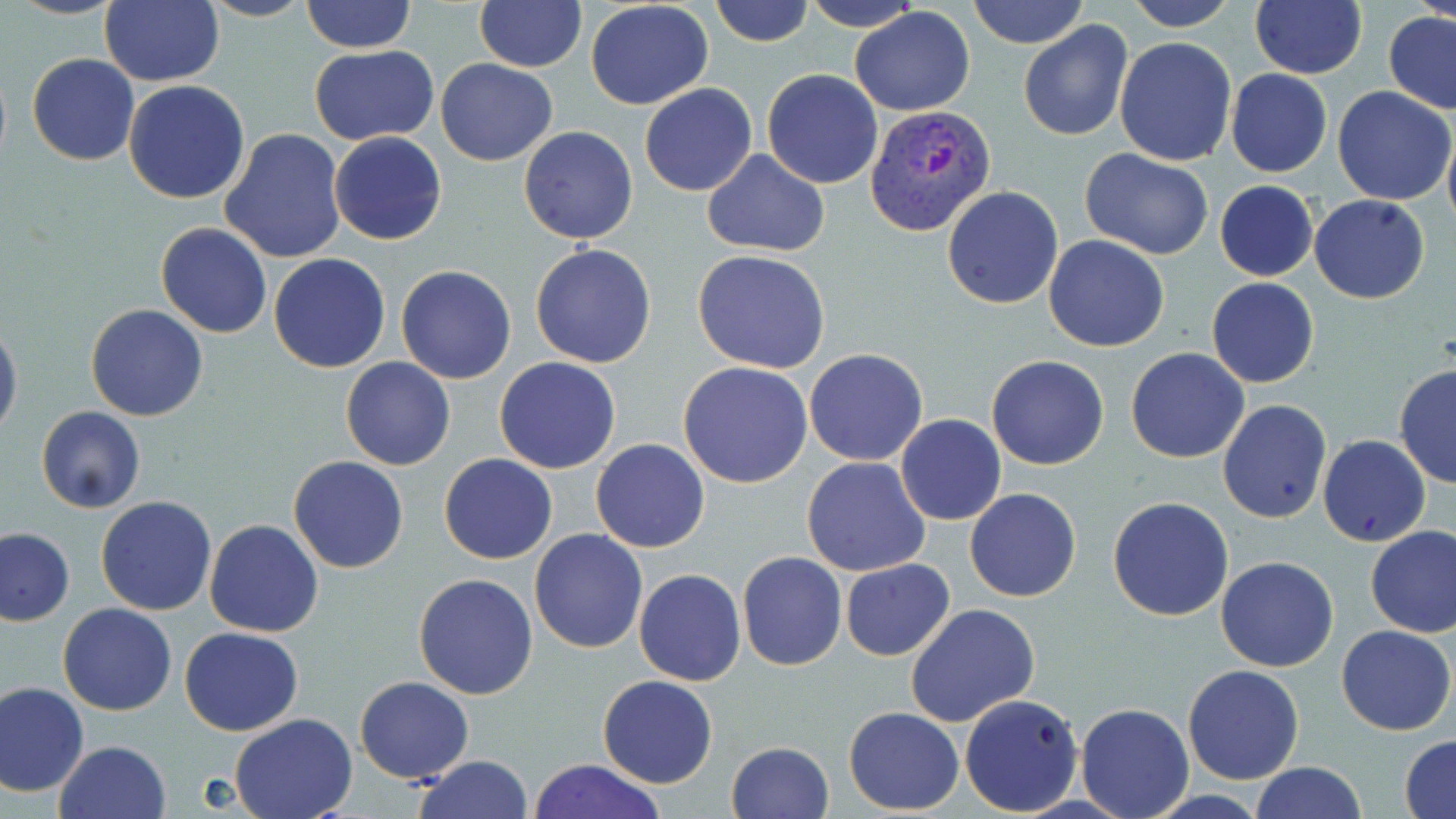

Summary:
  - Coordinate format: approximate bounding boxes as (x1, y1, x2, y2) in pixels
  - Plasmodium vivax-infected red blood cell locations: (865, 106, 995, 234)
  - Uninfected red blood cell locations: (11, 0, 126, 20), (199, 0, 316, 22), (302, 0, 415, 52), (474, 0, 586, 71), (711, 0, 814, 47), (967, 0, 1088, 49), (1123, 0, 1239, 30), (1248, 0, 1366, 79), (1414, 0, 1456, 26), (99, 1, 224, 87), (465, 1, 578, 154), (585, 1, 714, 111), (799, 2, 928, 30), (850, 6, 975, 117), (1383, 11, 1456, 114), (1019, 20, 1132, 141), (1114, 36, 1236, 166), (310, 46, 440, 144), (26, 52, 140, 166), (435, 58, 558, 167), (762, 68, 884, 188), (1225, 69, 1332, 177), (123, 80, 251, 204), (639, 83, 758, 196), (1331, 85, 1454, 206), (517, 126, 638, 245), (1443, 127, 1456, 235), (220, 128, 346, 265), (329, 132, 446, 246), (1081, 147, 1215, 259), (702, 150, 830, 257), (1214, 180, 1319, 282), (941, 185, 1063, 310), (1310, 194, 1430, 305), (156, 222, 272, 339), (1042, 235, 1169, 352), (530, 243, 657, 368), (693, 250, 832, 374), (269, 253, 390, 373), (396, 265, 518, 384), (1206, 278, 1319, 389), (85, 304, 209, 421), (0, 321, 22, 444), (1124, 347, 1250, 464), (804, 348, 928, 465), (987, 355, 1110, 470), (340, 357, 455, 470), (494, 357, 621, 474), (679, 361, 813, 488), (1392, 364, 1456, 489), (1217, 399, 1332, 524), (36, 405, 146, 514), (896, 414, 1006, 526), (1318, 434, 1430, 547), (590, 439, 710, 554), (439, 453, 557, 565), (288, 456, 409, 574), (801, 456, 931, 576), (965, 487, 1082, 602), (95, 496, 217, 616), (1108, 497, 1234, 622), (205, 520, 323, 637), (1365, 524, 1456, 637), (0, 528, 74, 625), (528, 528, 648, 654), (736, 551, 848, 672), (1216, 556, 1339, 672), (839, 559, 954, 661), (632, 568, 745, 686), (413, 572, 540, 699), (58, 603, 178, 716), (905, 603, 1040, 727), (1336, 625, 1454, 735), (179, 627, 303, 736), (1183, 665, 1303, 785), (355, 676, 473, 784), (598, 676, 718, 789), (1, 681, 89, 797), (959, 693, 1083, 816), (1076, 702, 1194, 817), (844, 707, 964, 814), (229, 713, 358, 819), (1401, 735, 1456, 818), (55, 740, 172, 819), (725, 741, 834, 819), (413, 755, 535, 819), (529, 758, 666, 819), (1251, 763, 1367, 818)
  - Slide-level diagnosis: Plasmodium vivax
  - Magnification: 1000x
  - Preparation: thin blood film
  - Modality: light microscopy
  - Image size: 1456×819 pixels
  - Field of view: single
  - Stain: May-Grünwald-Giemsa